Locate every P. falciparum parasite and identify its life-cycle stage.
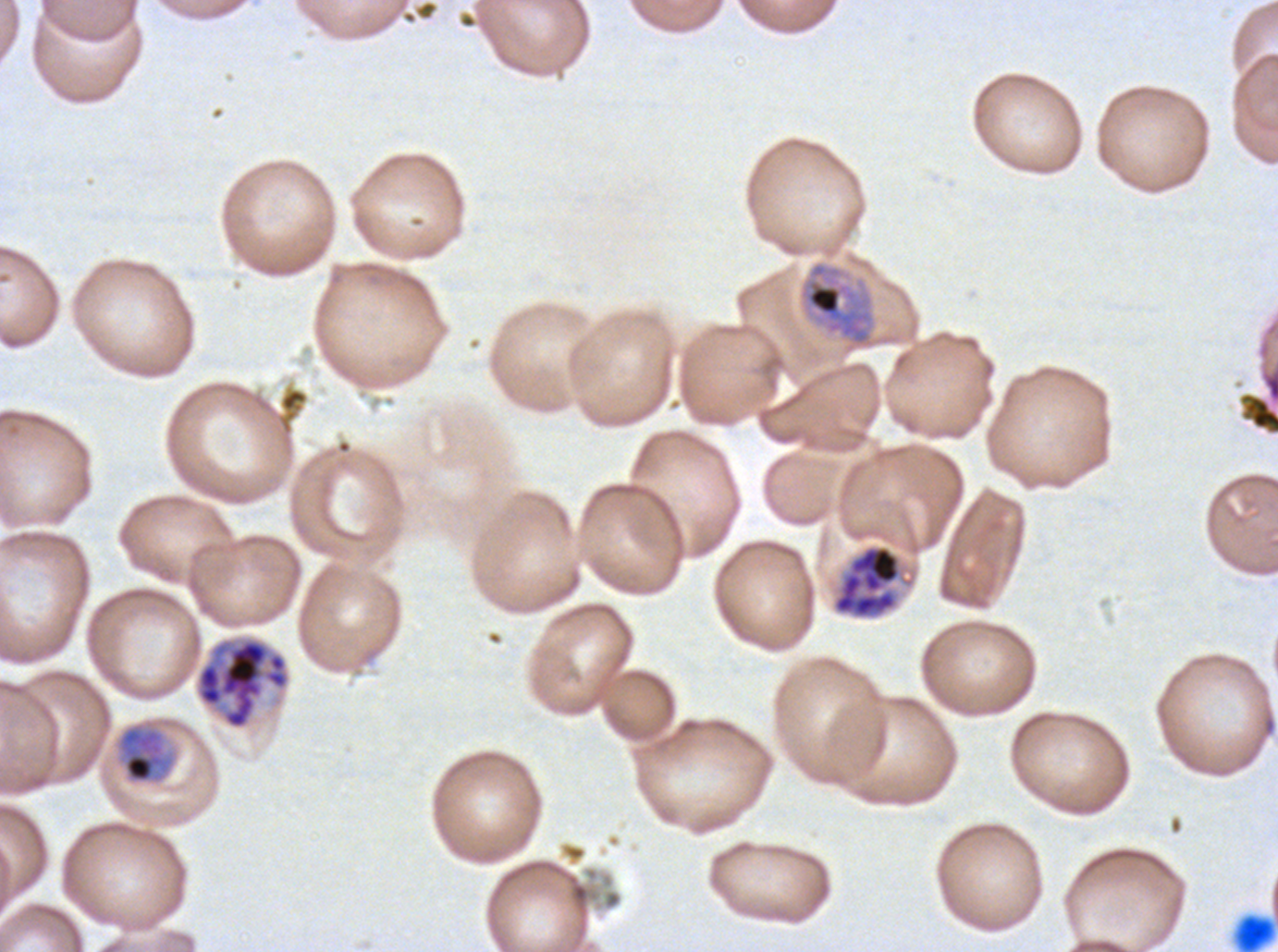

Approximate bounding boxes as (x1, y1, x2, y2) in pixels.
Mid trophozoites: (115, 721, 178, 785).
Late trophozoites: (803, 262, 873, 348).
Late schizonts: (832, 544, 902, 619), (195, 636, 290, 730).
No rings, late-ring/early-trophozoite forms, early schizonts, segmenters, or gametocytes observed.

debris_locations: 'approximate bounding boxes as (x1, y1, x2, y2) in pixels: (1238, 392, 1277, 435), (1234, 913, 1276, 951)'
preparation: thin blood film
field_of_view: one sub-image of a larger composite
life_cycle_stages_observed: mid trophozoite, late trophozoite, late schizont
stain: Giemsa
image_size: 1278×952 pixels
specimen: ex-vivo P. falciparum culture from a patient in The Gambia, grown for 24 to 48 hours